Assess this cell for malaria.
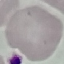
It is uninfected.

Photographed with a smartphone camera at the microscope eyepiece. Cell patch, automatically extracted from a larger field of view and resized to 64 × 64 pixels. Giemsa-stained preparation. Thin blood smear.